Assess this cell for malaria.
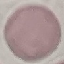
It is uninfected.

Automatically extracted cell patch, resized to 64 × 64 pixels. Giemsa stain. Thin blood film. Photographed with a smartphone camera at the microscope eyepiece.